Classify this cell by malaria status.
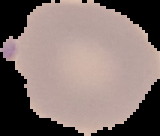

Parasitized.

image_type: segmented cell region with the area outside set to black
image_size: 160×136 pixels
preparation: thin blood smear